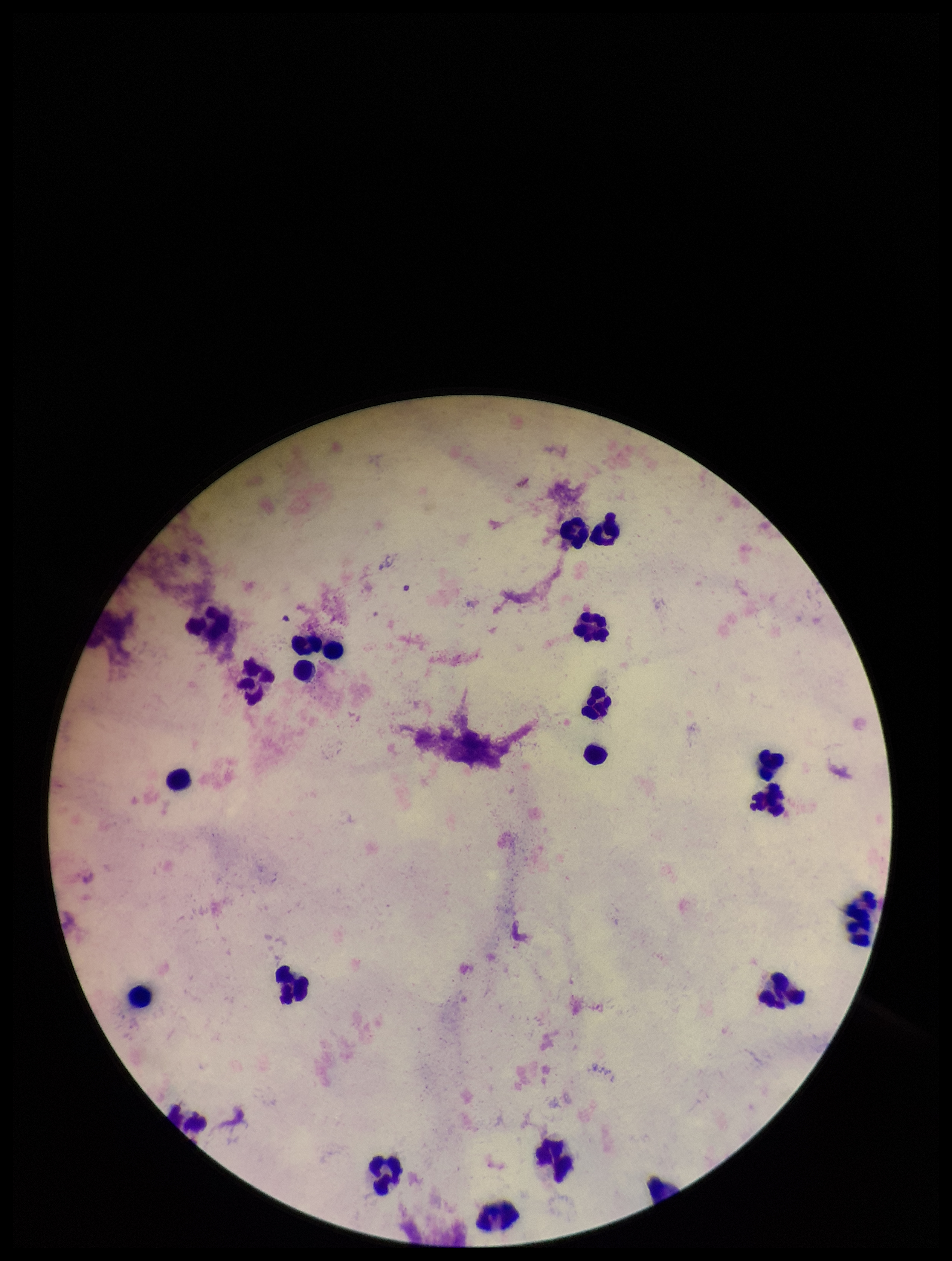 Leukocyte count: 22. Plasmodium parasites: none detected. Parasite count: 0. Smartphone photograph taken through the eyepiece of a microscope. Image is 952×1261 pixels. Patient malaria status: negative. Stained with Giemsa. Preparation: thick smear. One field from this slide.